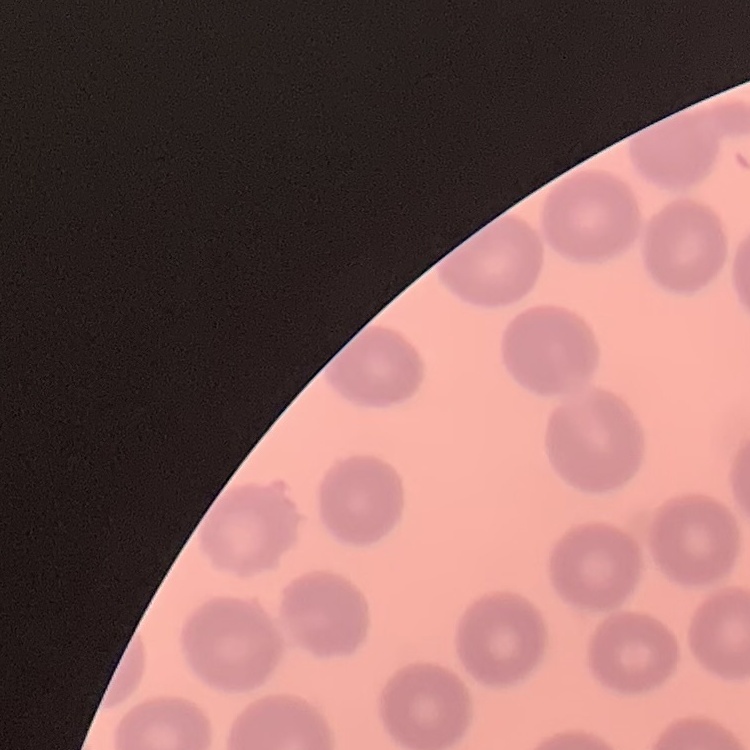
The erythrocytes show no rouleaux formation. Thin peripheral smear. Field's or Giemsa stain. Square crop of a larger photomicrograph.